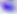
modality = micrograph
magnification = 400x
identification = Toxoplasma gondii